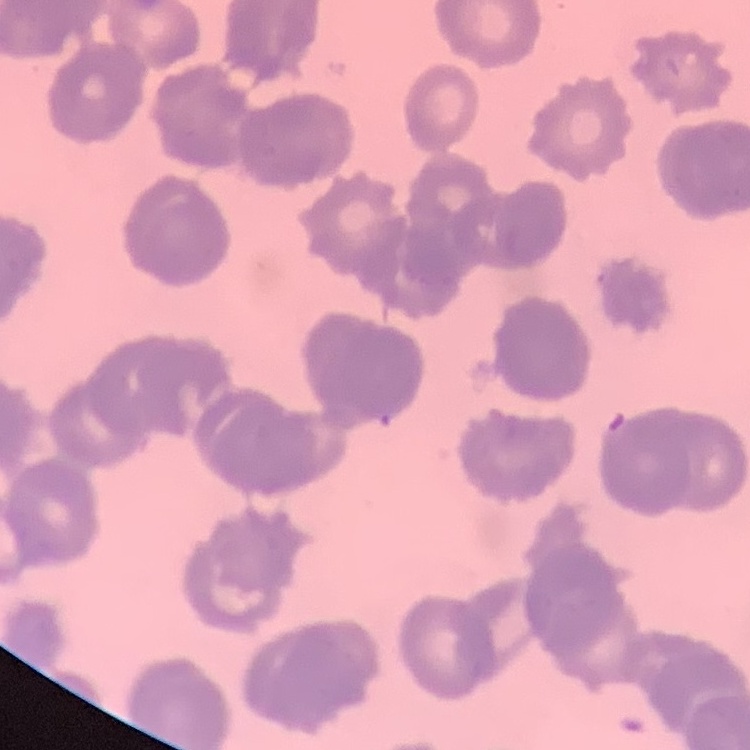

Summary:
  - Erythrocyte morphology: rouleaux formation
  - Image type: square crop of a larger photomicrograph
  - Stain: Field's or Giemsa
  - Preparation: thin blood smear